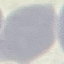
Result: no malaria parasites seen. Cell patch, automatically extracted from a larger field of view and resized to 64 × 64 pixels. Thin blood smear. Giemsa-stained preparation. Photographed with a smartphone camera at the microscope eyepiece.